Assess for malaria.
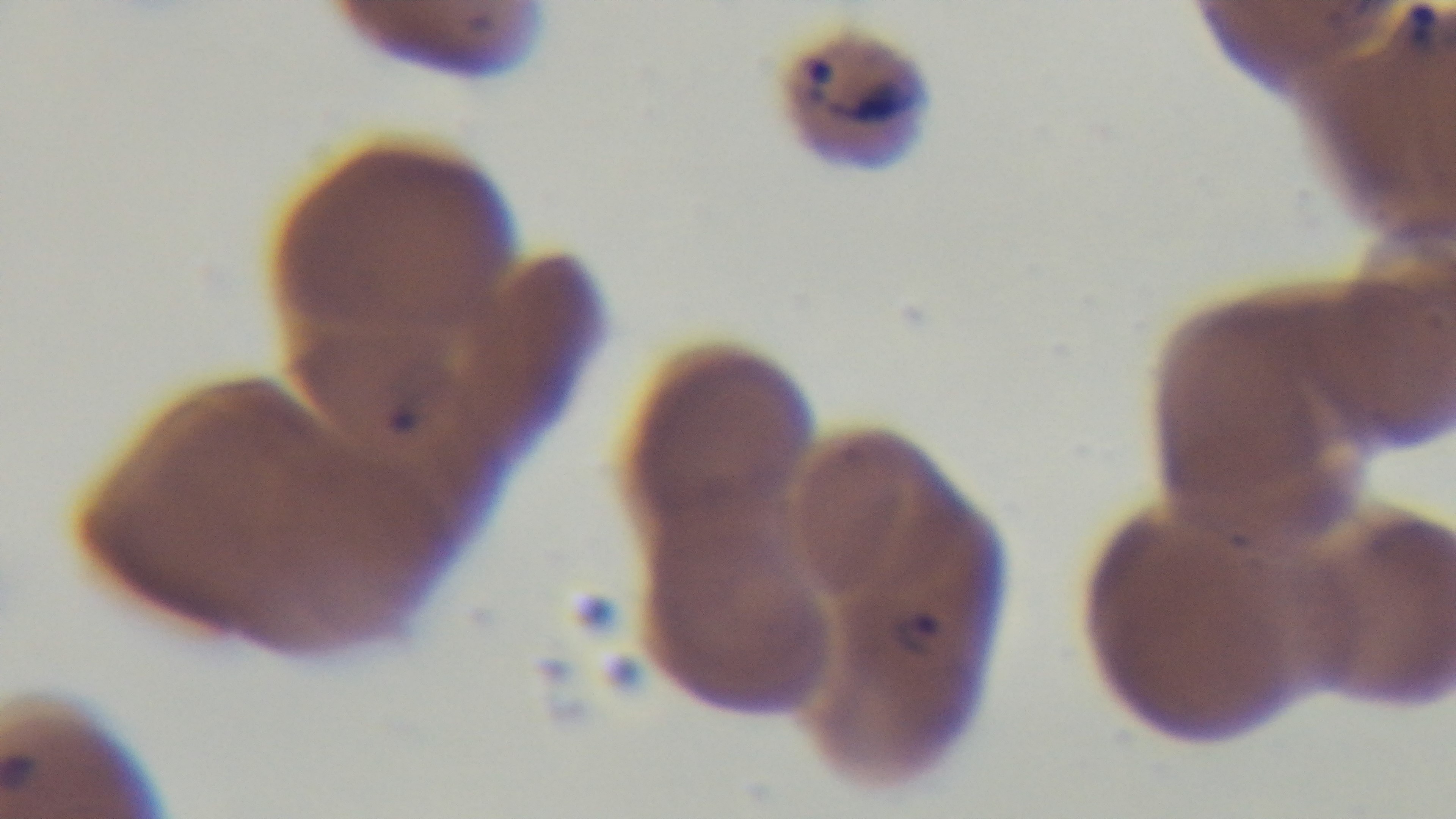
It is infected.

Single field of view. Oil-immersion objective, 100x. Captured with a mounted 4K digital camera. Preparation: thin blood film. Photomicrograph. Giemsa stain.